Comment on the morphology of the erythrocytes.
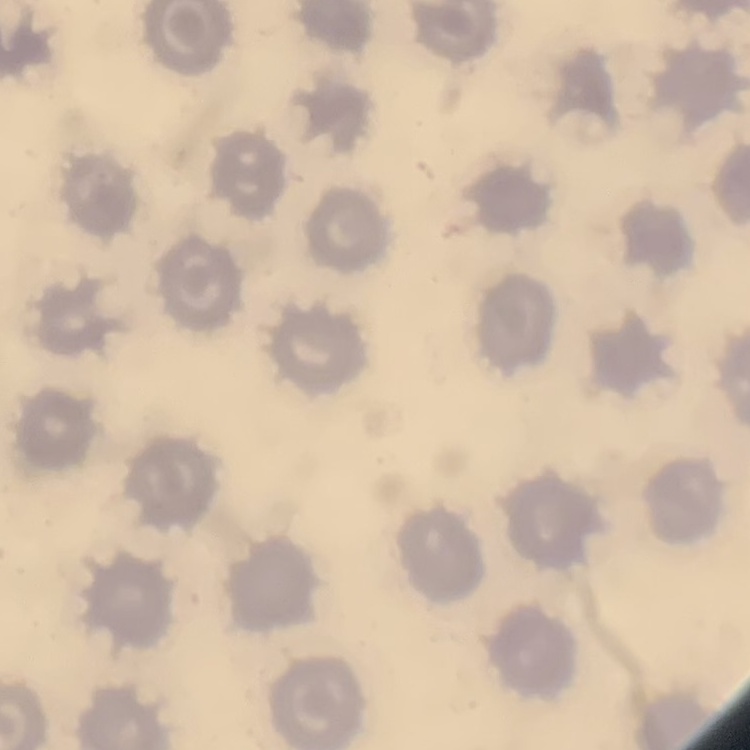

They show no rouleaux formation.

Summary:
  - Preparation: thin blood film
  - Image type: one tile cut from a larger photomicrograph
  - Stain: Field's or Giemsa